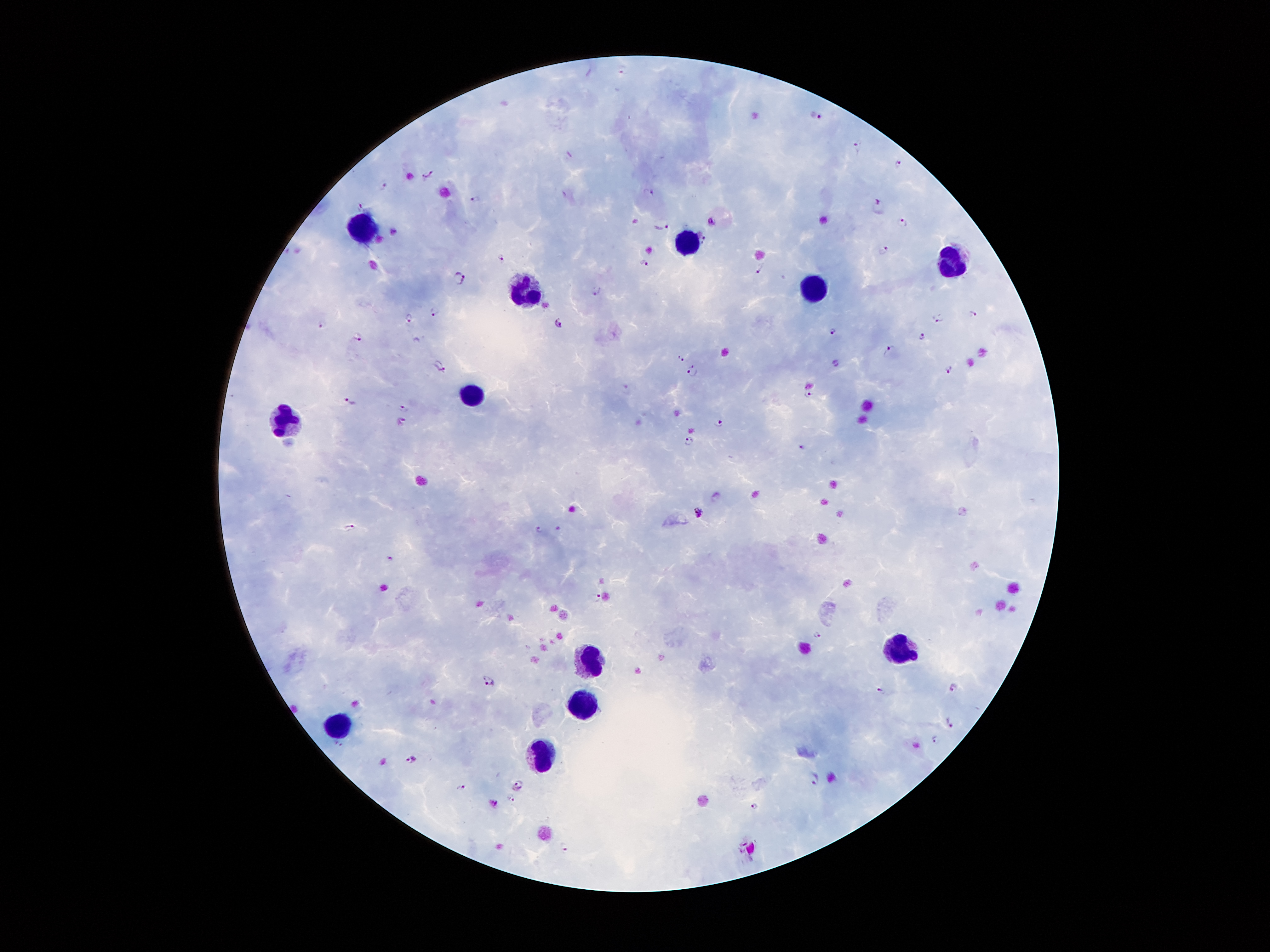

Approximate centers as [x, y] in pixels. Leukocyte locations: [367, 227], [686, 243], [955, 263], [817, 286], [528, 290], [470, 392], [285, 415], [894, 648], [590, 660], [583, 698], [338, 722], [541, 757]. Malaria parasite locations: [816, 115], [859, 145], [570, 154], [899, 163], [428, 174], [384, 186], [649, 192], [477, 200], [362, 204], [879, 206], [711, 221], [904, 223], [663, 224], [394, 231], [704, 240], [883, 251], [501, 257], [644, 263], [758, 271], [460, 278], [596, 292], [435, 310], [973, 313], [409, 317], [941, 318], [560, 323], [323, 324], [833, 329], [359, 336], [923, 336], [891, 351], [681, 359], [837, 364], [440, 366], [693, 369], [950, 369], [625, 390], [809, 394], [349, 400], [404, 409], [401, 421], [720, 422], [688, 441], [802, 446], [699, 512], [350, 527], [538, 529], [391, 559], [597, 596], [818, 635], [489, 679], [954, 687], [882, 691], [949, 723], [936, 739], [411, 758], [815, 778], [521, 780], [461, 788], [510, 799], [753, 807], [564, 847]. 100x magnification. Smartphone photograph taken through the microscope eyepiece. Giemsa stain. Single field of view. Patient malaria status: positive for Plasmodium falciparum. Image is 1270×952 pixels. Thick blood film.